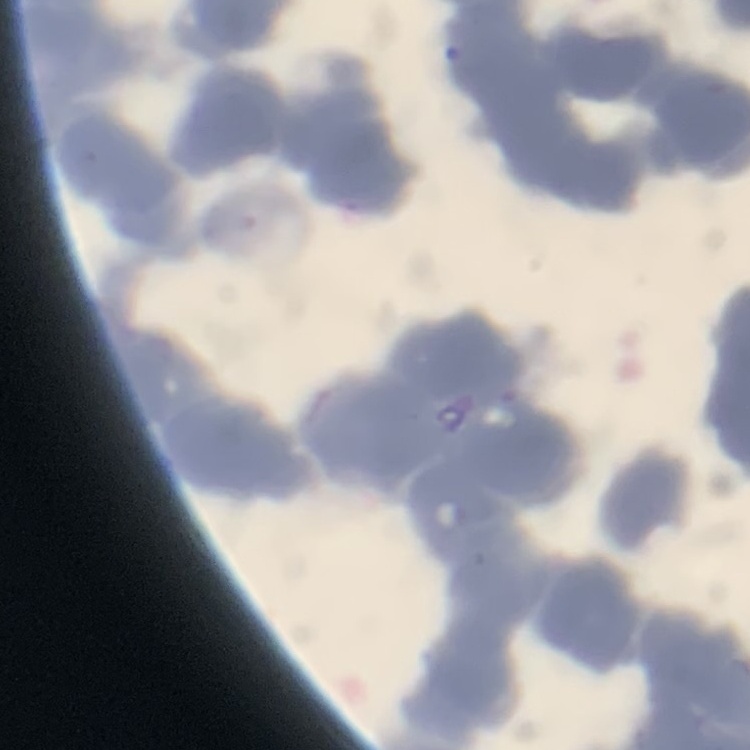
Summary:
  - Erythrocyte morphology: rouleaux formation
  - Stain: Field's or Giemsa
  - Preparation: thin blood smear
  - Image type: square crop of a larger photomicrograph